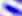

Summary:
  - Modality: micrograph
  - Magnification: 400x
  - Identification: Toxoplasma gondii